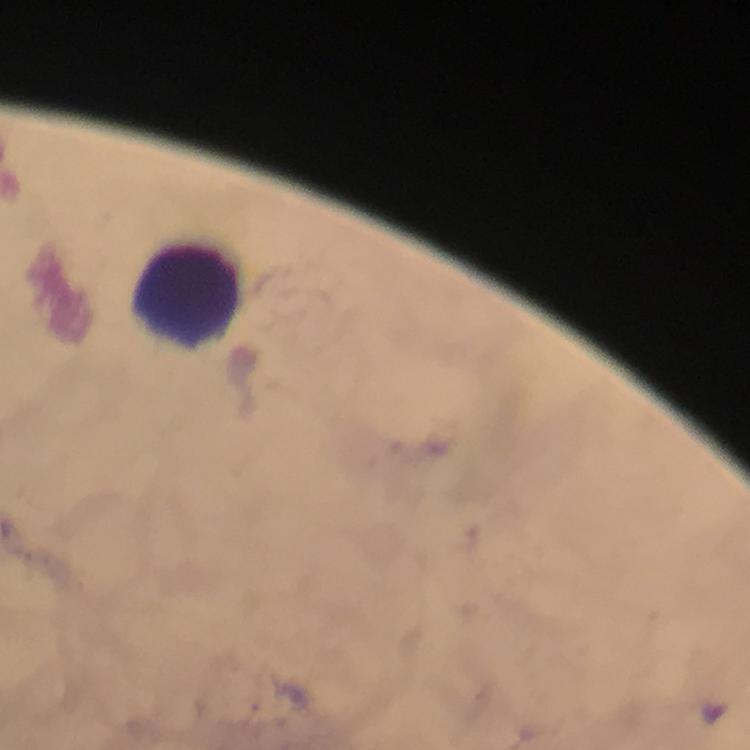
Approximate centers as [x, y] in pixels.
Summary:
  - Leukocyte locations: [185, 292]
  - Preparation: thick blood film
  - Capture: smartphone mounted on the microscope
  - Stain: Giemsa
  - Plasmodium parasites: none seen
  - Image size: 750×750 pixels
  - Magnification: 100x
  - Context: from a malaria diagnostic workup
  - Cropped from: a single field of view
  - Immersion oil: applied